Point out every malaria parasite and every leukocyte.
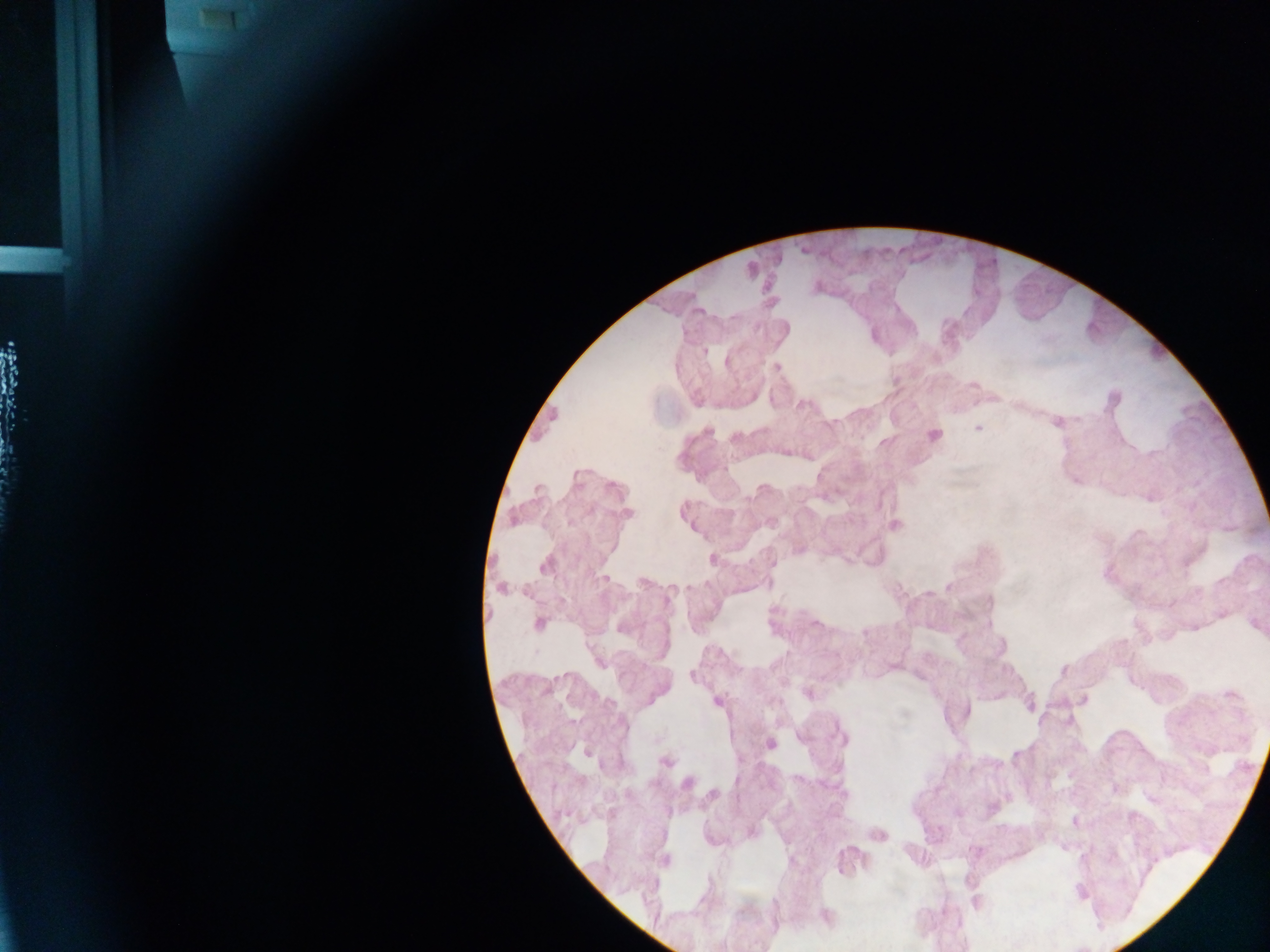

Approximate centers as {x, y} in pixels.
Malaria parasites: {704, 351}, {777, 367}, {978, 429}, {708, 431}, {934, 435}, {544, 566}, {501, 588}, {539, 624}, {691, 676}, {664, 762}, {687, 784}.
No leukocytes observed.

capture = mobile-phone photograph through a microscope
country = Ghana
image size = 1270×952 pixels
preparation = thick blood smear
field of view = single